Identify the parasite.
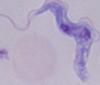
A trypanosome.

modality = photomicrograph
magnification = 1000x